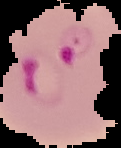

Segmented cell region on a black background. From a thin blood smear. Image is 121×148 pixels. Result: malaria parasites detected.